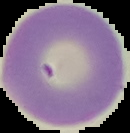

Cell region segmented out of the field of view; the surrounding area is masked to black. From a thin blood film. Malaria status: uninfected. Image is 130×133 pixels.